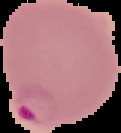
Image is 121×133 pixels. Malaria status: parasitized. Segmented cell region on a black background. From a thin blood film.